Classify this cell by malaria status.
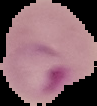

Parasitized.

Summary:
  - Preparation: thin blood smear
  - Image size: 97×106 pixels
  - Image type: segmented cell region on a black background